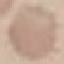 Result: negative for malaria parasites. Cell patch, automatically extracted from a larger field of view and resized to 64 × 64 pixels. Giemsa-stained preparation. Photographed with a smartphone camera at the microscope eyepiece. Thin blood smear.